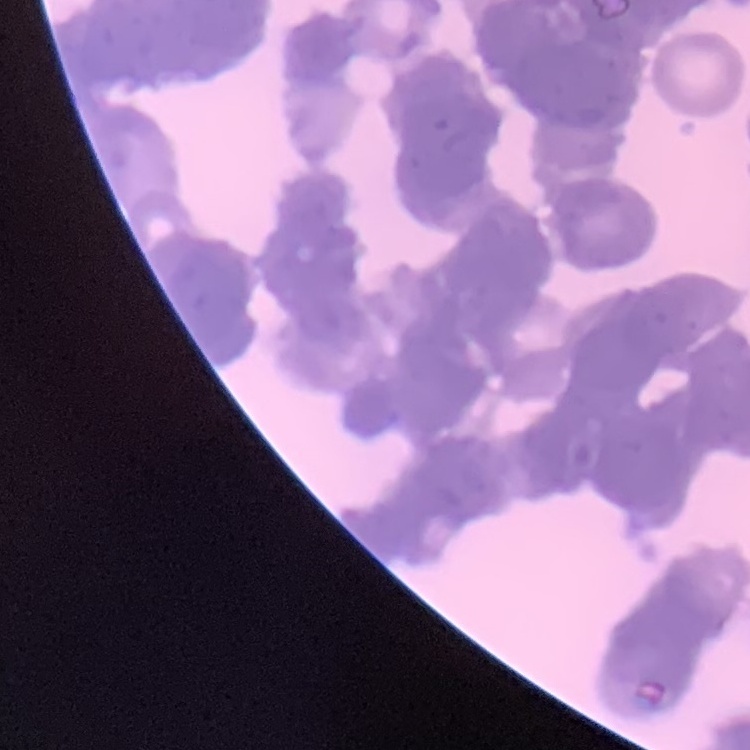

The red blood cells exhibit rouleaux formation. Thin blood smear. Field's or Giemsa stain. Square crop of a larger photomicrograph.